Find each parasitized RBC.
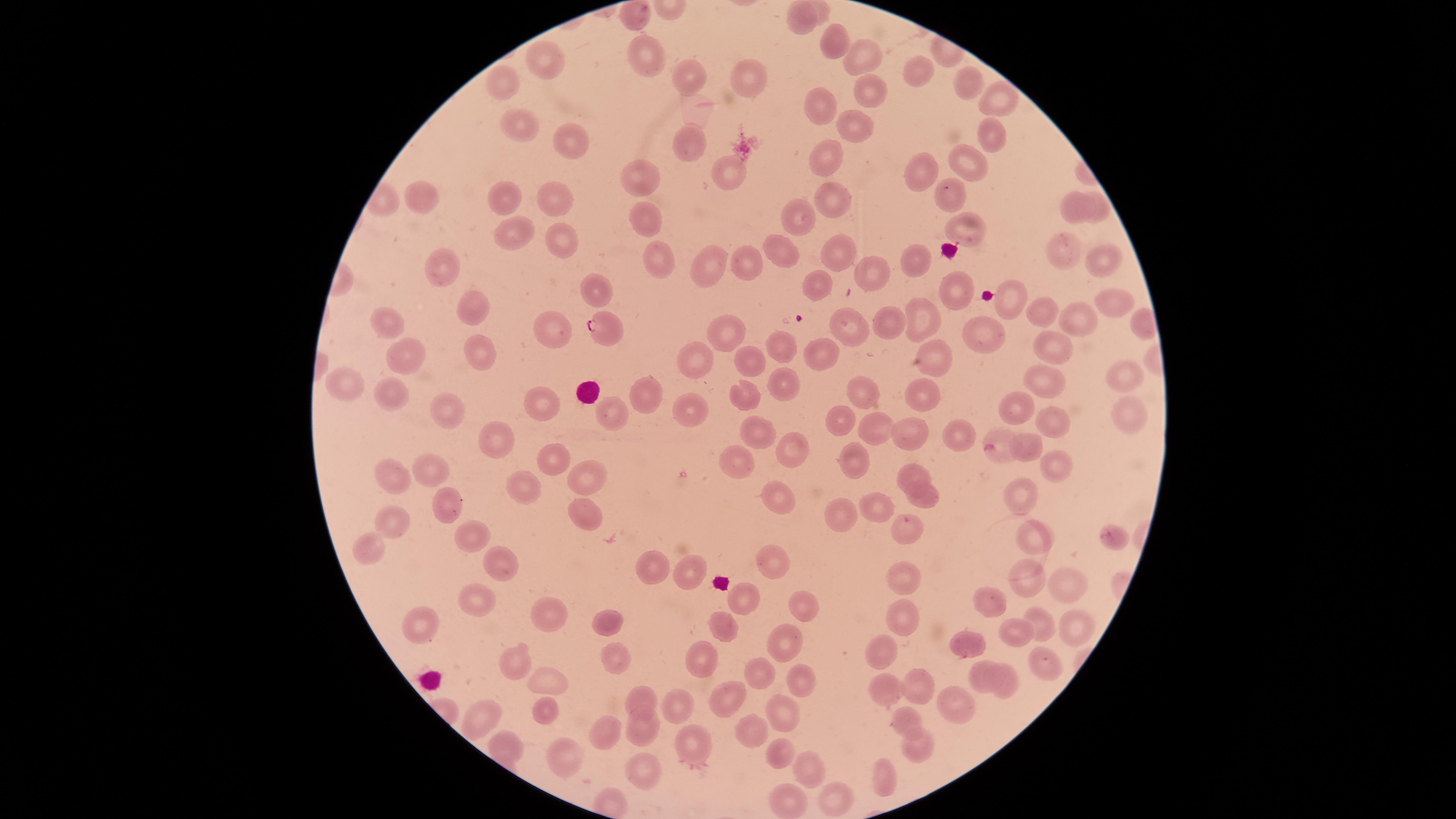
Approximate marker points as {x, y} in pixels.
Parasitized RBCs: {608, 327}.

Approximate marker points as {x, y} in pixels.
Summary:
  - Uninfected RBCs: {634, 16}, {798, 19}, {832, 43}, {648, 50}, {862, 52}, {544, 63}, {918, 71}, {693, 76}, {746, 78}, {966, 83}, {504, 84}, {863, 89}, {1001, 98}, {816, 102}, {851, 120}, {519, 122}, {988, 132}, {691, 144}, {566, 145}, {823, 157}, {969, 162}, {914, 168}, {726, 171}, {644, 179}, {943, 190}, {832, 196}, {427, 197}, {499, 201}, {553, 205}, {1099, 206}, {1077, 208}, {801, 215}, {645, 219}, {966, 229}, {512, 233}, {562, 237}, {1062, 247}, {787, 252}, {843, 252}, {654, 253}, {910, 256}, {1104, 257}, {743, 260}, {709, 261}, {862, 269}, {443, 271}, {820, 281}, {600, 291}, {953, 293}, {1016, 300}, {1115, 301}, {475, 310}, {1050, 311}, {919, 313}, {388, 317}, {1089, 320}, {894, 321}, {729, 326}, {555, 327}, {842, 327}, {983, 337}, {782, 347}, {477, 348}, {1055, 351}, {819, 354}, {946, 355}, {415, 356}, {701, 356}, {747, 360}, {1123, 378}, {1035, 379}, {351, 383}, {784, 385}, {859, 388}, {398, 394}, {645, 396}, {747, 397}, {920, 397}, {1011, 399}, {540, 401}, {440, 407}, {615, 407}, {696, 407}, {842, 416}, {1134, 416}, {1051, 417}, {874, 424}, {757, 426}, {915, 428}, {995, 431}, {967, 433}, {1025, 438}, {495, 441}, {789, 445}, {550, 456}, {737, 460}, {858, 462}, {1051, 463}, {426, 464}, {909, 471}, {593, 477}, {396, 479}, {524, 492}, {780, 492}, {924, 493}, {443, 498}, {1022, 499}, {877, 503}, {589, 511}, {836, 518}, {905, 521}, {393, 522}, {473, 533}, {1112, 540}, {1042, 541}, {371, 546}, {777, 560}, {503, 564}, {646, 569}, {686, 573}, {899, 573}, {1025, 575}, {1059, 575}, {738, 596}, {483, 602}, {994, 605}, {801, 609}, {550, 614}, {907, 614}, {615, 618}, {1045, 621}, {1082, 622}, {429, 623}, {719, 627}, {1017, 633}, {787, 636}, {966, 641}, {605, 653}, {876, 653}, {515, 656}, {1051, 657}, {700, 659}, {758, 674}, {800, 674}, {982, 677}, {1007, 679}, {916, 681}, {543, 683}, {882, 683}, {725, 698}, {642, 700}, {954, 703}, {682, 704}, {781, 710}, {544, 711}, {906, 712}, {480, 713}, {645, 726}, {605, 727}, {750, 728}, {923, 740}, {507, 742}, {563, 752}, {694, 756}, {779, 757}, {806, 767}, {633, 770}, {882, 782}, {832, 794}, {790, 800}
  - Field of view: single
  - Stain: Giemsa
  - Image size: 1456×819 pixels
  - Preparation: thin blood smear
  - Capture: smartphone photograph through the microscope eyepiece
  - Visible region: circular
  - Species: Plasmodium falciparum